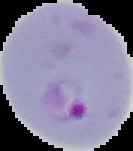 From a thin blood smear. Result: Plasmodium parasites detected. Image is 133×151 pixels. Cell region segmented out of the field of view; the surrounding area is masked to black.